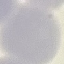
result = negative for malaria parasites
stain = Giemsa
image type = cell patch, automatically extracted from a larger field of view and resized to 64 × 64 pixels
preparation = thin blood film
capture = smartphone through the microscope eyepiece